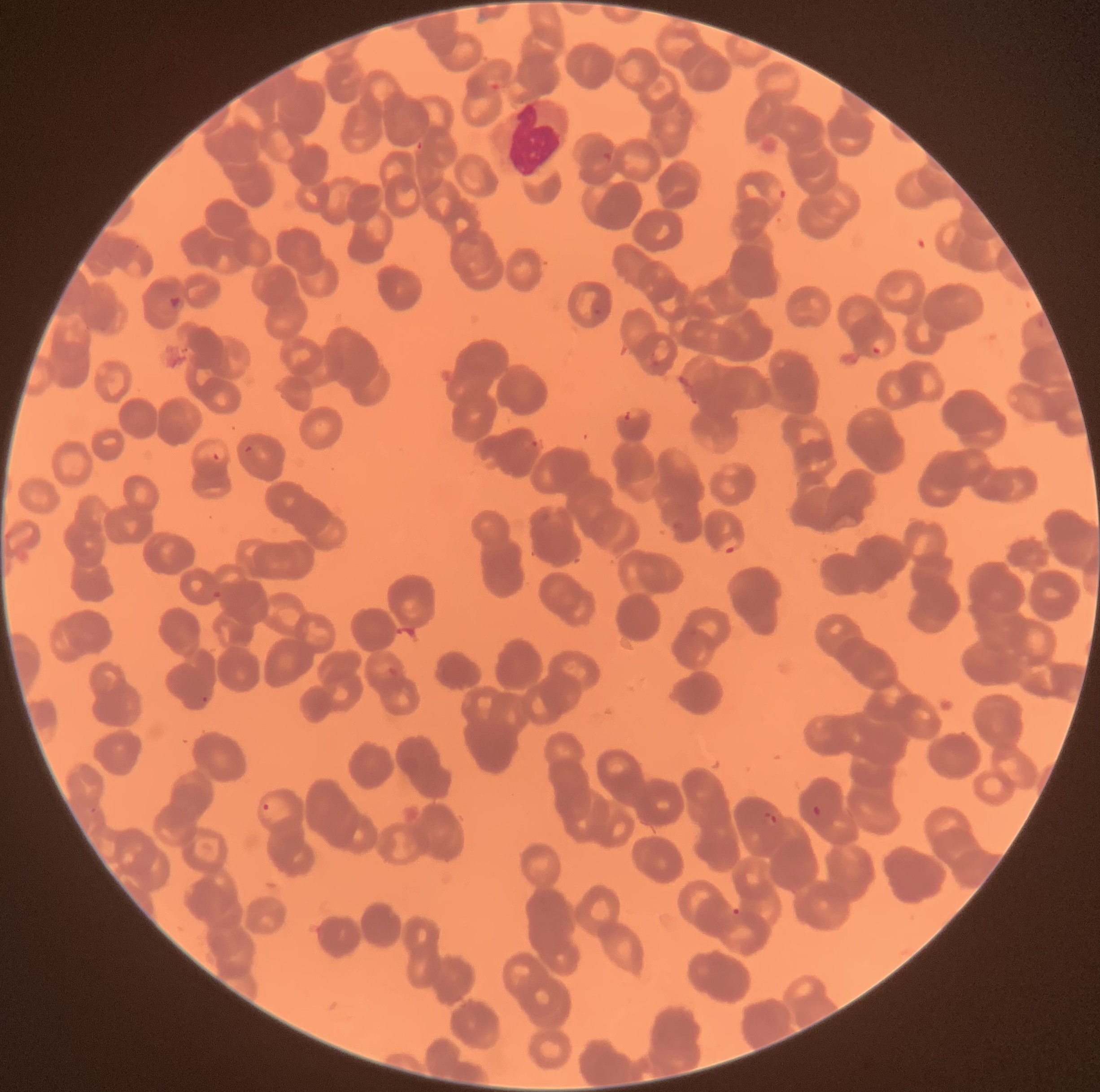
Summary:
  - Coordinate format: approximate bounding boxes as named x1/y1/x2/y2 corners in pixels
  - White blood cell locations: (x1=488, y1=98, x2=572, y2=175)
  - Plasmodium parasite locations: (x1=603, y1=152, x2=613, y2=165), (x1=767, y1=183, x2=788, y2=202), (x1=168, y1=295, x2=184, y2=311), (x1=592, y1=307, x2=603, y2=317), (x1=870, y1=337, x2=891, y2=355), (x1=624, y1=410, x2=633, y2=422), (x1=531, y1=440, x2=539, y2=448), (x1=243, y1=444, x2=254, y2=457), (x1=211, y1=451, x2=221, y2=462), (x1=718, y1=536, x2=742, y2=553), (x1=212, y1=590, x2=222, y2=601), (x1=201, y1=694, x2=209, y2=705), (x1=262, y1=802, x2=271, y2=811), (x1=812, y1=805, x2=821, y2=816), (x1=90, y1=806, x2=97, y2=814), (x1=762, y1=811, x2=779, y2=826), (x1=731, y1=907, x2=742, y2=916)
  - Image size: 1100×1092 pixels
  - Red blood cell morphology: rouleaux formation
  - Modality: optical microscopy
  - Preparation: thin blood smear